Assess this cell for malaria.
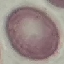

It is uninfected.

Thin smear of blood. Cell patch, automatically extracted from a larger field of view and resized to 64 × 64 pixels. Photographed with a smartphone camera at the microscope eyepiece. Giemsa-stained preparation.